Give the position of every leukocyte visible.
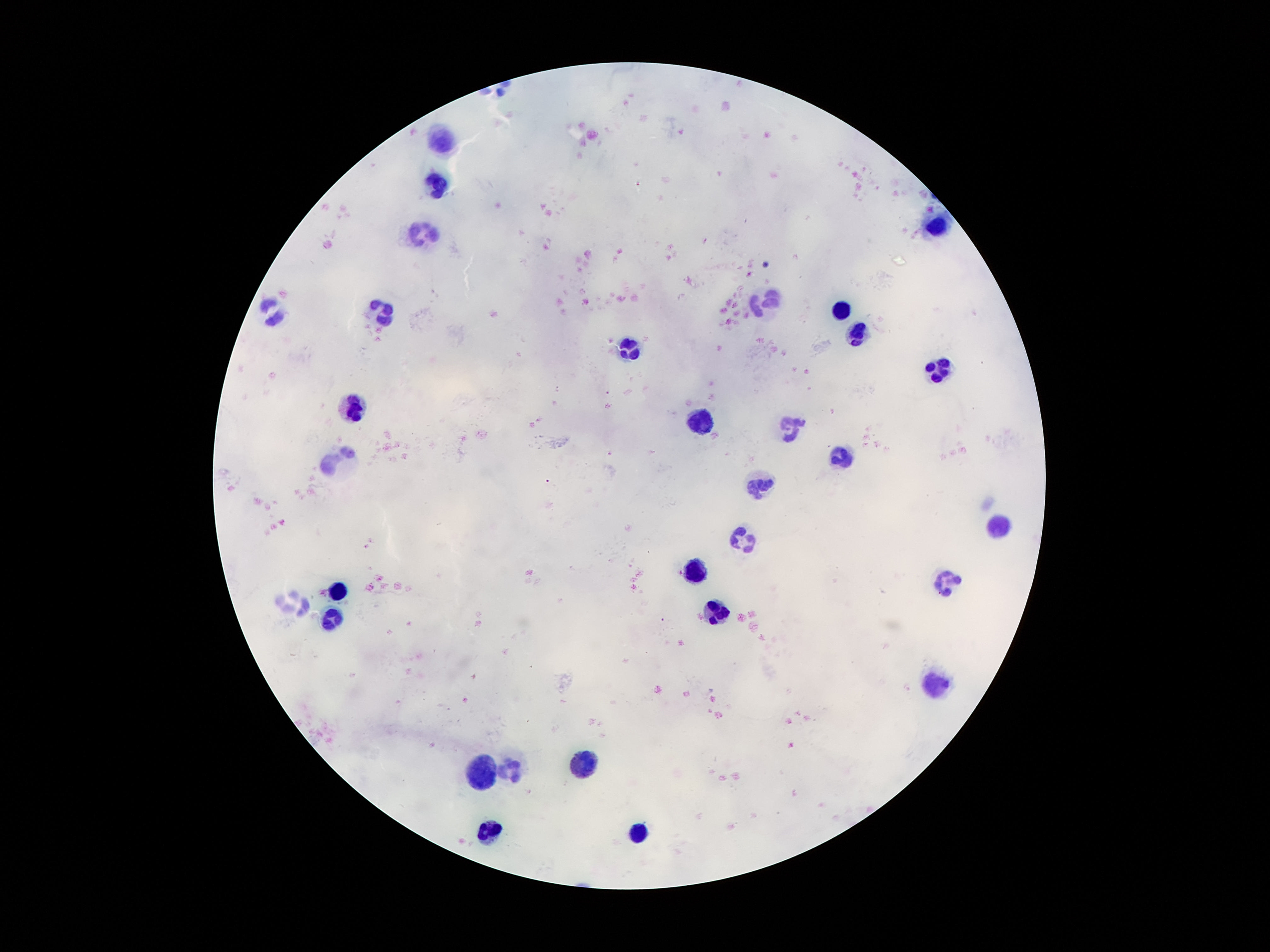

Approximate centers as (x, y) in pixels.
Leukocytes: (445, 136), (433, 183), (937, 228), (419, 232), (767, 297), (843, 310), (273, 311), (382, 312), (857, 336), (630, 345), (943, 367), (353, 403), (699, 418), (791, 427), (839, 455), (335, 461), (757, 482), (998, 525), (744, 537), (697, 570), (949, 582), (335, 592), (294, 601), (716, 610), (331, 617), (937, 682), (585, 762), (511, 766), (482, 770), (488, 830), (638, 831).

Patient malaria status: negative. One field from this slide. Thick blood film. Image is 1270×952 pixels. Giemsa stain. 100x magnification. Smartphone photograph taken through the microscope eyepiece.